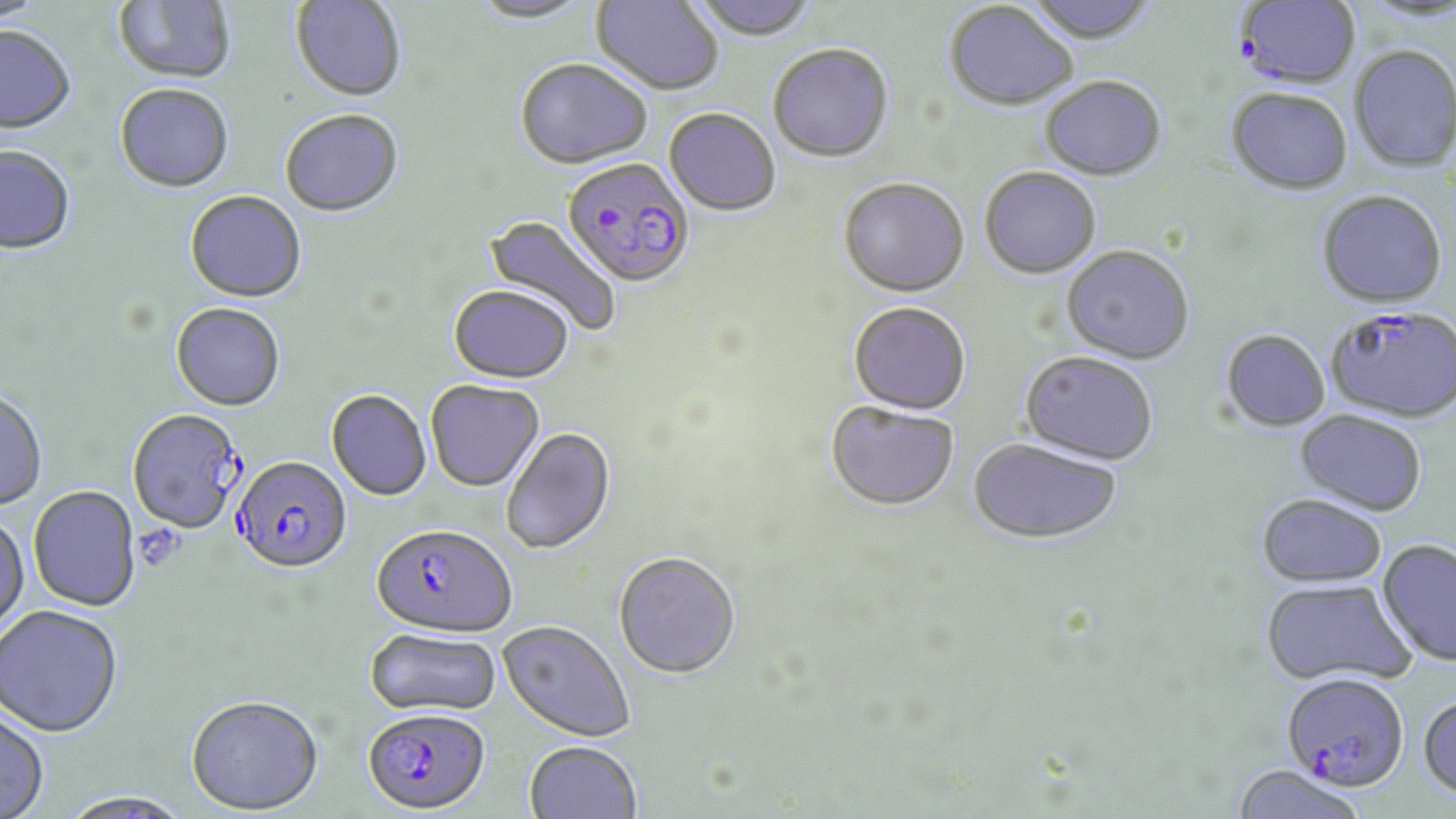

slide-level diagnosis = Plasmodium falciparum
field of view = one of a larger specimen
modality = light microscopy
magnification = 1000x
image size = 1456×819 pixels
Plasmodium falciparum-infected red blood cell locations = approximate bounding boxes as named x1/y1/x2/y2 corners in pixels: (x1=1234, y1=1, x2=1362, y2=92), (x1=562, y1=159, x2=695, y2=291), (x1=1326, y1=306, x2=1455, y2=424), (x1=127, y1=409, x2=245, y2=535), (x1=232, y1=455, x2=352, y2=574), (x1=372, y1=524, x2=517, y2=638), (x1=1280, y1=671, x2=1409, y2=791), (x1=362, y1=706, x2=491, y2=814)
uninfected red blood cell locations = approximate bounding boxes as named x1/y1/x2/y2 corners in pixels: (x1=0, y1=0, x2=47, y2=26), (x1=114, y1=0, x2=236, y2=86), (x1=291, y1=0, x2=407, y2=103), (x1=468, y1=0, x2=596, y2=26), (x1=590, y1=0, x2=724, y2=97), (x1=689, y1=0, x2=820, y2=42), (x1=1022, y1=0, x2=1159, y2=47), (x1=944, y1=3, x2=1078, y2=113), (x1=0, y1=28, x2=76, y2=137), (x1=768, y1=43, x2=894, y2=164), (x1=1349, y1=48, x2=1455, y2=173), (x1=515, y1=60, x2=653, y2=171), (x1=1040, y1=78, x2=1166, y2=183), (x1=115, y1=85, x2=234, y2=195), (x1=1226, y1=90, x2=1353, y2=198), (x1=664, y1=108, x2=781, y2=217), (x1=280, y1=110, x2=404, y2=219), (x1=0, y1=147, x2=76, y2=257), (x1=979, y1=168, x2=1101, y2=281), (x1=838, y1=179, x2=969, y2=300), (x1=1316, y1=191, x2=1447, y2=310), (x1=185, y1=192, x2=307, y2=304), (x1=482, y1=214, x2=622, y2=337), (x1=1061, y1=247, x2=1195, y2=366), (x1=449, y1=287, x2=574, y2=385), (x1=170, y1=303, x2=285, y2=412), (x1=847, y1=303, x2=971, y2=417), (x1=1219, y1=330, x2=1331, y2=433), (x1=1018, y1=352, x2=1158, y2=467), (x1=426, y1=380, x2=544, y2=492), (x1=0, y1=388, x2=48, y2=512), (x1=326, y1=390, x2=432, y2=501), (x1=825, y1=402, x2=959, y2=512), (x1=1294, y1=410, x2=1427, y2=516), (x1=501, y1=427, x2=616, y2=555), (x1=967, y1=439, x2=1124, y2=547), (x1=28, y1=486, x2=141, y2=612), (x1=1256, y1=493, x2=1388, y2=588), (x1=0, y1=513, x2=29, y2=637), (x1=1377, y1=538, x2=1456, y2=667), (x1=613, y1=551, x2=741, y2=679), (x1=1260, y1=578, x2=1416, y2=688), (x1=0, y1=605, x2=123, y2=737), (x1=498, y1=620, x2=635, y2=742), (x1=364, y1=626, x2=502, y2=717), (x1=1418, y1=692, x2=1456, y2=803), (x1=186, y1=693, x2=324, y2=814), (x1=0, y1=704, x2=50, y2=818), (x1=523, y1=740, x2=643, y2=819), (x1=1228, y1=765, x2=1371, y2=819), (x1=58, y1=791, x2=195, y2=819)
stain = May-Grünwald-Giemsa
preparation = thin blood smear
platelet locations = approximate bounding boxes as named x1/y1/x2/y2 corners in pixels: (x1=132, y1=522, x2=186, y2=573)